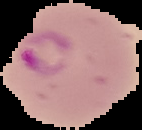
malaria status = parasitized
preparation = thin blood smear
image type = segmented cell region with the area outside set to black
image size = 142×130 pixels